Evaluate for malaria.
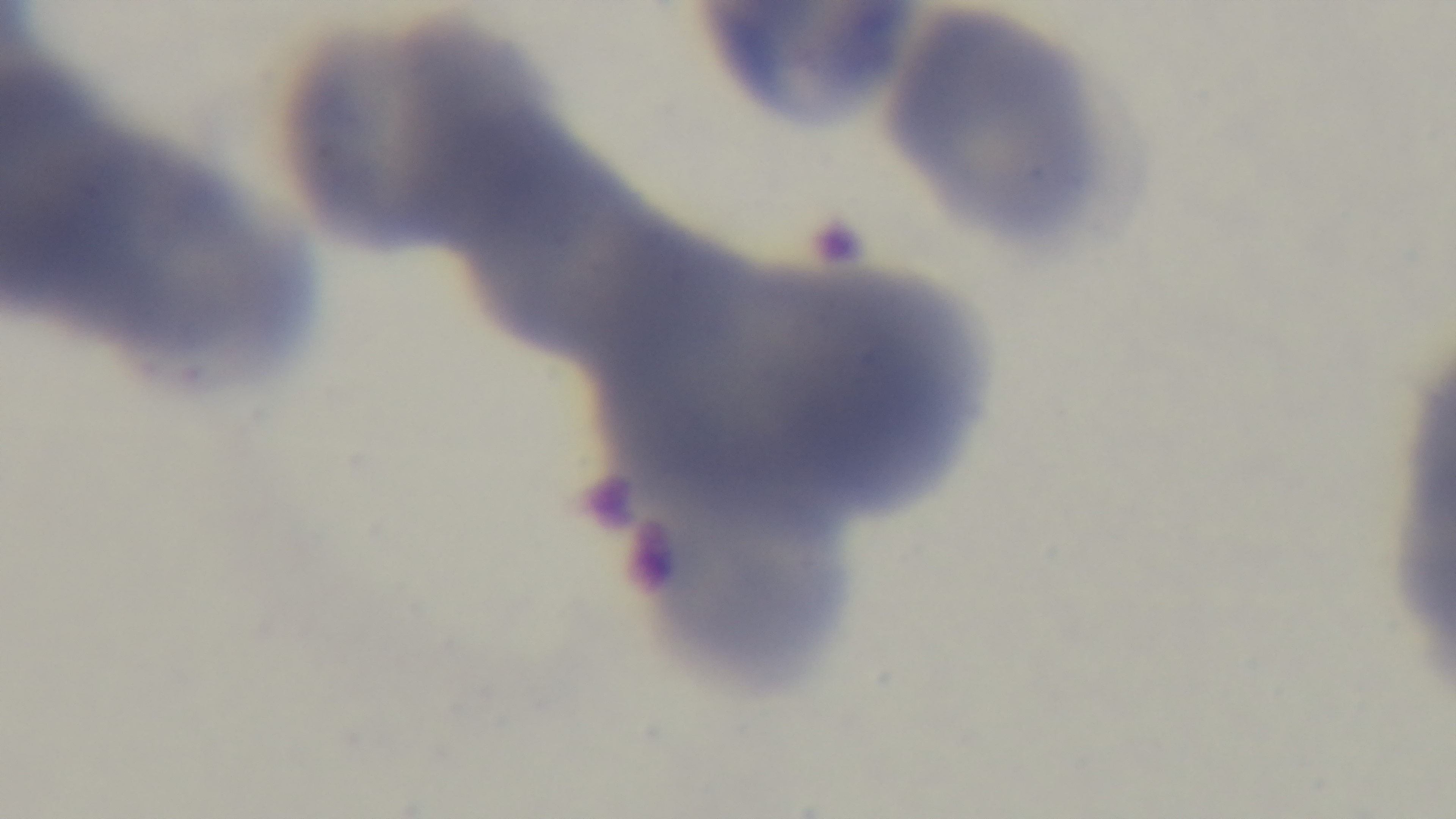

It is uninfected.

Photomicrograph. Oil-immersion objective, 100x. Giemsa-stained. Single field of view. Preparation: thin. Mounted 4K digital camera.